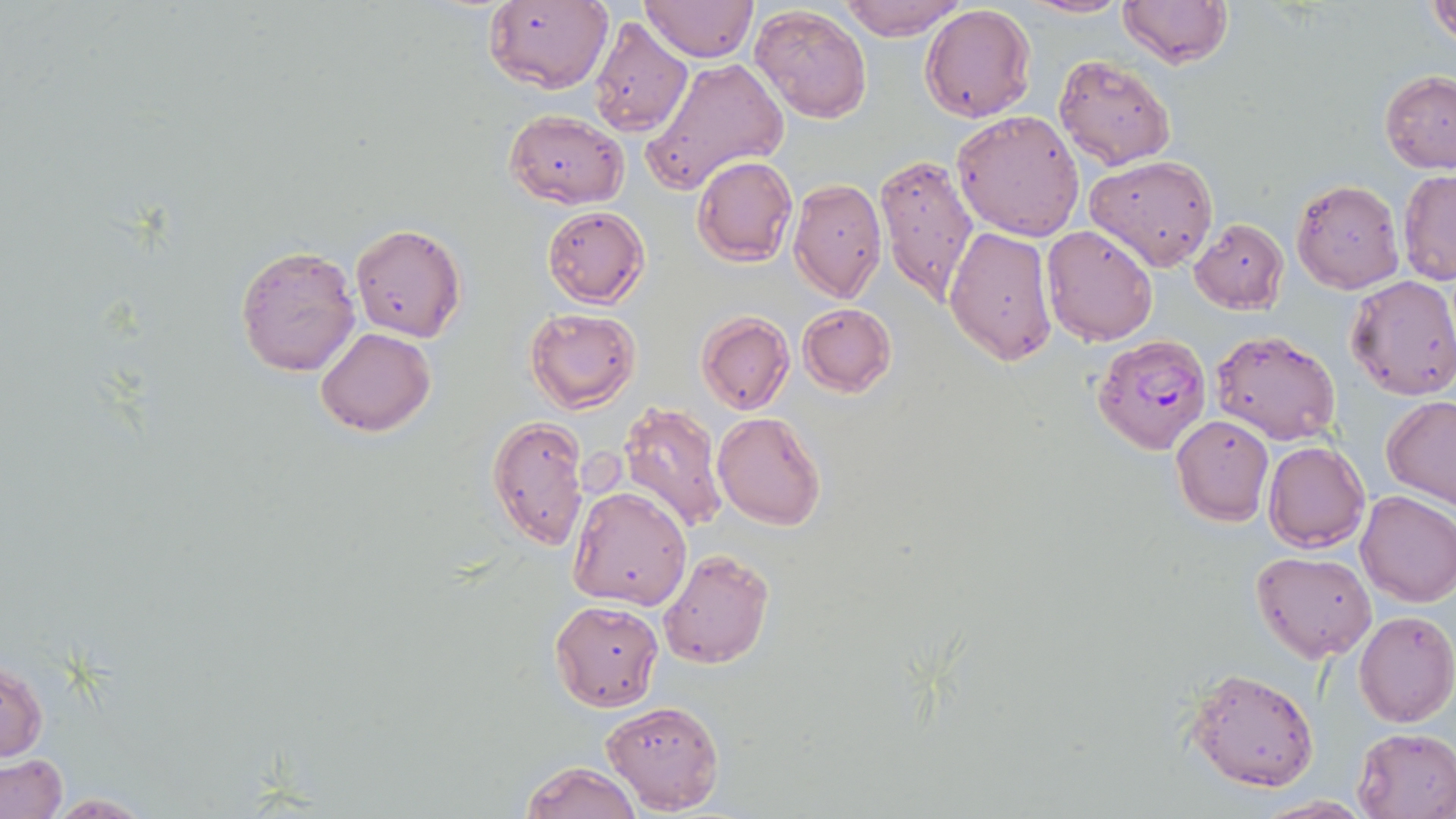

{
  "slide_level_diagnosis": "Plasmodium falciparum",
  "preparation": "thin blood smear",
  "magnification": "1000x",
  "stain": "May-Grünwald-Giemsa",
  "image_size": "1456×819 pixels",
  "uninfected_red_blood_cell_locations": "approximate bounding boxes as (x1, y1, x2, y2) in pixels: (639, 0, 760, 64), (839, 0, 966, 41), (1018, 0, 1132, 18), (1117, 0, 1232, 68), (482, 2, 612, 93), (1426, 2, 1456, 45), (749, 4, 871, 122), (919, 5, 1036, 123), (590, 15, 693, 139), (1053, 54, 1176, 170), (641, 57, 790, 196), (1378, 70, 1456, 174), (504, 109, 629, 207), (951, 110, 1085, 240), (874, 152, 980, 303), (1084, 154, 1219, 271), (692, 155, 798, 266), (1398, 169, 1456, 285), (787, 177, 887, 303), (1292, 178, 1404, 294), (542, 206, 650, 307), (1189, 218, 1288, 314), (349, 222, 467, 342), (943, 225, 1057, 365), (1041, 225, 1158, 346), (235, 245, 360, 376), (1346, 274, 1456, 400), (798, 303, 896, 396), (525, 307, 641, 413), (696, 312, 794, 414), (316, 326, 435, 437), (1211, 328, 1342, 445), (1381, 395, 1456, 508), (618, 400, 727, 534), (712, 411, 827, 531), (1171, 414, 1275, 526), (486, 416, 588, 549), (1263, 440, 1370, 552), (567, 485, 692, 610), (1356, 489, 1456, 607), (659, 548, 775, 667), (1250, 549, 1378, 662), (549, 599, 663, 711), (1354, 611, 1456, 727), (1, 658, 48, 763), (1187, 666, 1319, 791), (600, 700, 725, 813), (1353, 727, 1456, 818), (1, 754, 67, 817), (519, 760, 643, 818), (42, 793, 159, 817), (1254, 796, 1377, 818)",
  "modality": "optical microscopy",
  "field_of_view": "single",
  "plasmodium_falciparum_infected_red_blood_cell_locations": "approximate bounding boxes as (x1, y1, x2, y2) in pixels: (1094, 335, 1212, 456)"
}